Name the parasite shown.
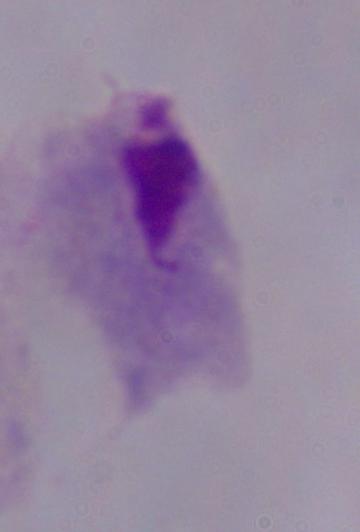
A trichomonad.

Photomicrograph. 1000x magnification.